Identify the parasite.
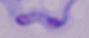

A trypanosome.

{
  "magnification": "1000x",
  "modality": "photomicrograph"
}